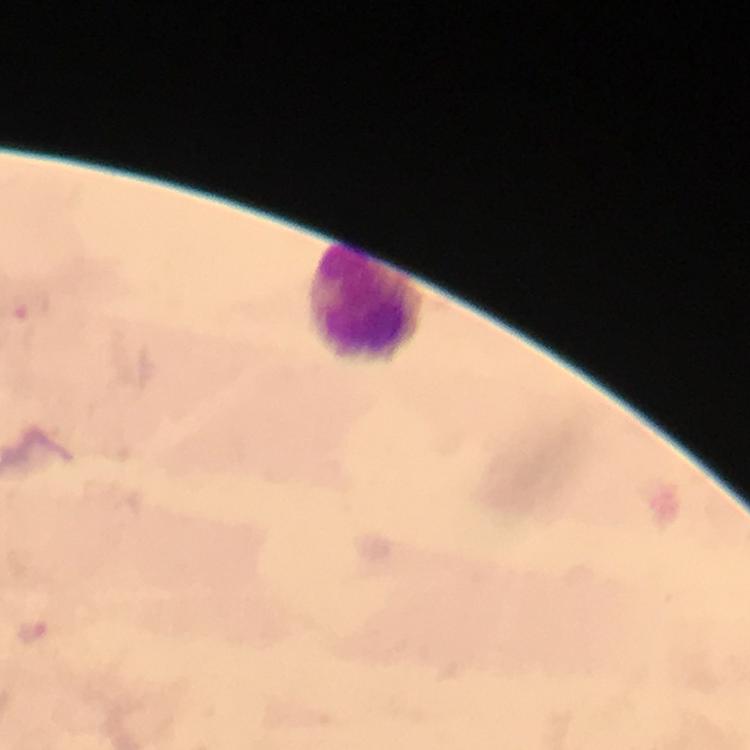

Approximate object centers, in pixels from the top-left corner. Plasmodium parasite locations: (x=33, y=310), (x=33, y=629). Leukocyte locations: (x=367, y=303). At 100x magnification. From a malaria diagnostic workup. Cropped region of a single field of view. Immersion oil applied. Image is 750×750 pixels. Thick blood film. Giemsa-stained preparation. Photographed with a smartphone mounted on the microscope.